Report the malaria status.
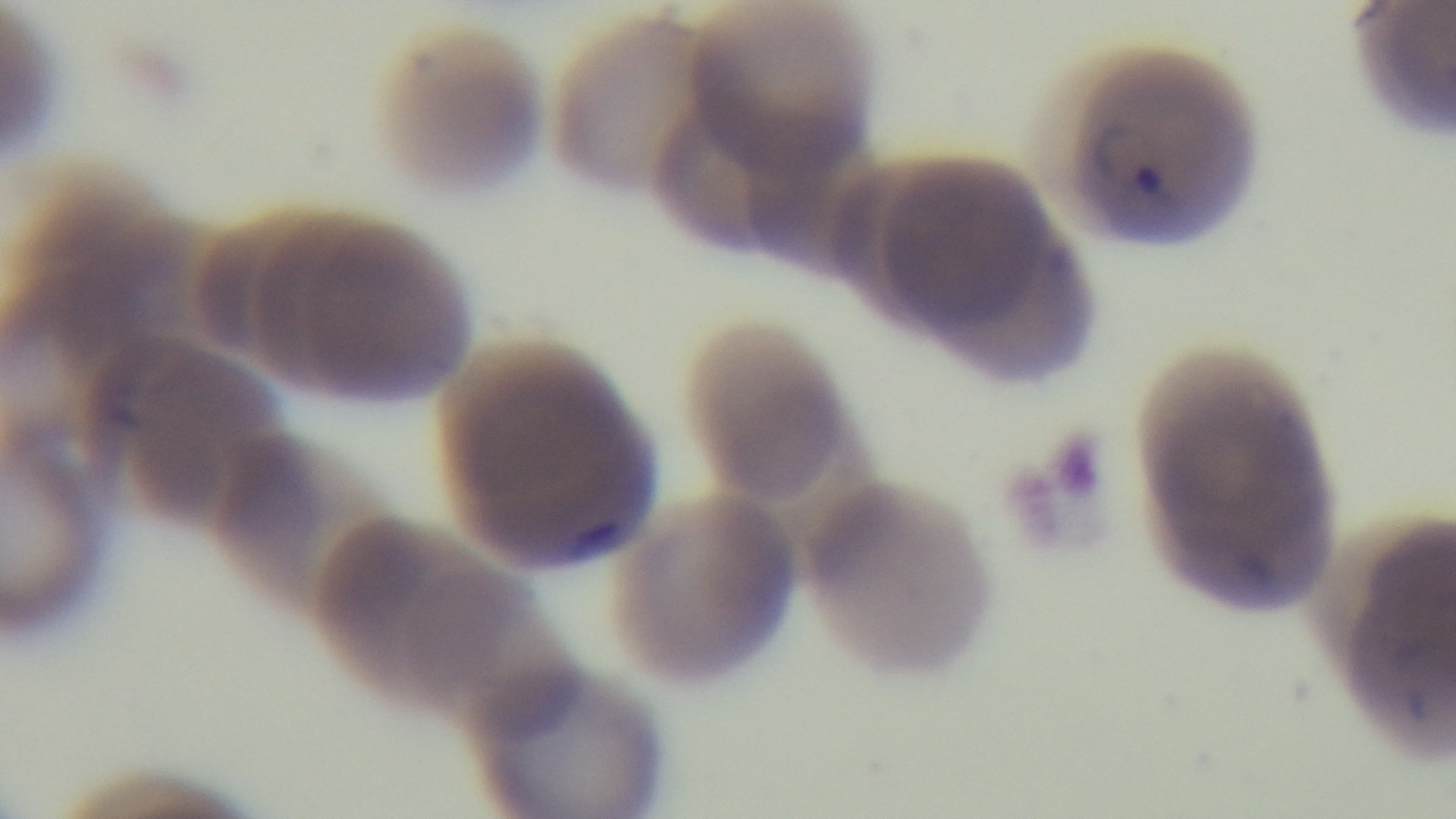
Infected.

Summary:
  - Capture: mounted 4K digital camera
  - Stain: Giemsa
  - Field of view: single
  - Objective: 100x oil immersion
  - Modality: light microscopy
  - Preparation: thin blood film